Assess the morphology of the erythrocytes.
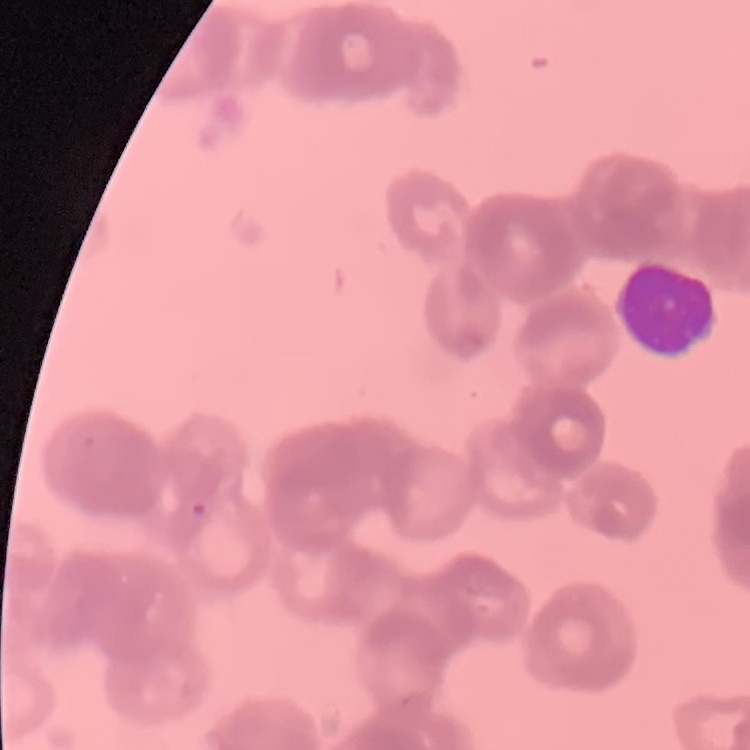

They show rouleaux formation.

stain = Field's or Giemsa
preparation = thin peripheral smear
image type = square crop of a larger photomicrograph